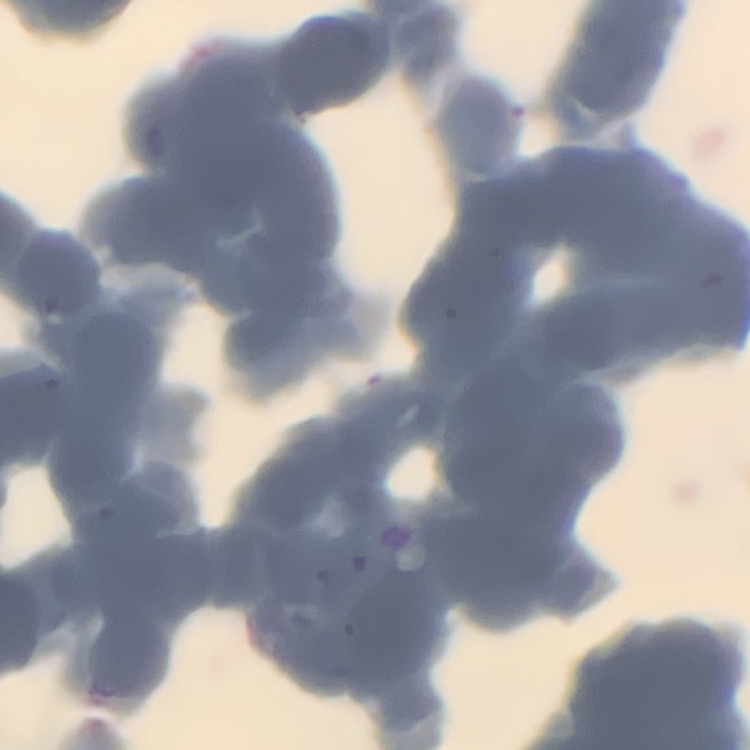

erythrocyte morphology = rouleaux formation
stain = Field's or Giemsa
preparation = thin peripheral smear
image type = one tile cut from a larger photomicrograph